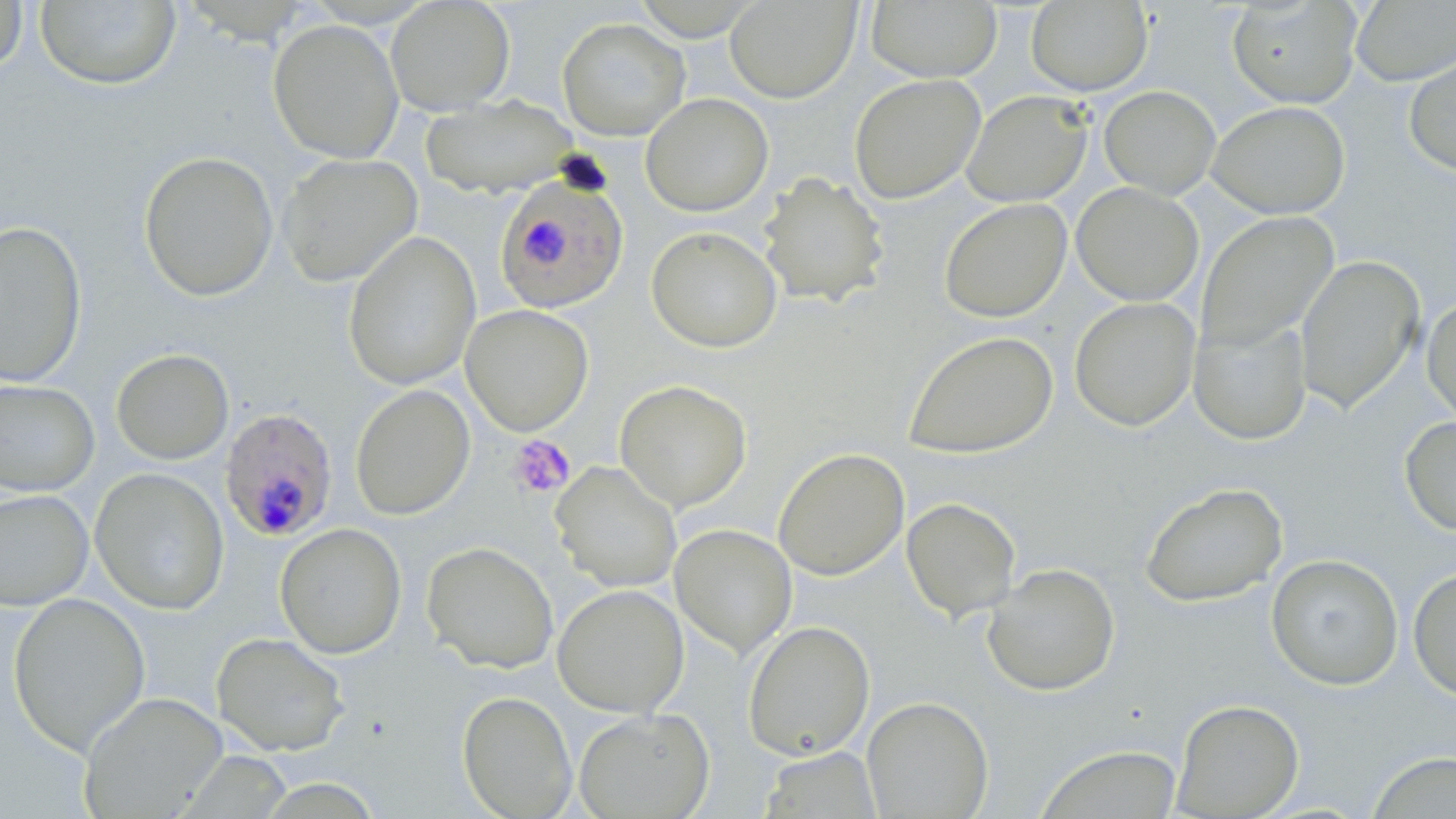

Approximate bounding boxes as [x1, y1, x2, y2] in pixels. Platelet locations: [508, 435, 576, 498]. Plasmodium falciparum-infected red blood cell locations: [494, 173, 630, 314], [219, 408, 338, 542]. Uninfected red blood cell locations: [386, 0, 515, 115], [724, 0, 861, 104], [1227, 0, 1362, 108], [0, 1, 28, 74], [36, 1, 182, 89], [866, 1, 1002, 83], [1025, 1, 1152, 95], [1351, 1, 1456, 85], [179, 2, 320, 46], [556, 17, 690, 141], [268, 20, 404, 163], [1403, 49, 1456, 177], [849, 74, 986, 204], [1099, 85, 1221, 199], [961, 90, 1092, 207], [641, 93, 773, 217], [420, 96, 578, 198], [1207, 100, 1350, 219], [138, 151, 279, 302], [277, 153, 422, 287], [757, 172, 890, 308], [1071, 182, 1204, 306], [939, 198, 1072, 323], [1196, 212, 1339, 352], [0, 219, 88, 387], [646, 225, 782, 353], [342, 230, 481, 391], [1295, 254, 1425, 413], [1421, 296, 1456, 428], [1069, 297, 1200, 431], [460, 305, 594, 436], [1189, 317, 1312, 445], [902, 330, 1059, 459], [111, 348, 234, 464], [0, 379, 100, 496], [614, 379, 752, 512], [349, 384, 475, 520], [1399, 415, 1456, 537], [773, 447, 910, 580], [550, 461, 683, 593], [90, 467, 230, 615], [1139, 481, 1289, 607], [0, 489, 93, 610], [901, 497, 1021, 621], [275, 523, 407, 658], [670, 524, 797, 658], [421, 541, 559, 674], [1265, 553, 1404, 690], [982, 563, 1121, 697], [1408, 565, 1456, 702], [552, 584, 689, 717], [8, 592, 150, 755], [742, 620, 875, 761], [212, 632, 350, 756], [457, 691, 578, 818], [78, 692, 228, 818], [861, 696, 994, 819], [1172, 699, 1304, 818], [573, 708, 714, 819], [1034, 744, 1184, 819], [759, 747, 882, 818], [1366, 751, 1456, 817]. Slide-level diagnosis: Plasmodium falciparum. Single field of view. May-Grünwald-Giemsa stain. Optical microscopy. Thin blood film. Captured at 1000x magnification. Image is 1456×819 pixels.